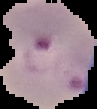
{
  "result": "Plasmodium parasites detected",
  "preparation": "thin blood film",
  "image_type": "cell region segmented out of the field of view; surrounding area masked to black",
  "image_size": "97×109 pixels"
}